State the blood parasite species.
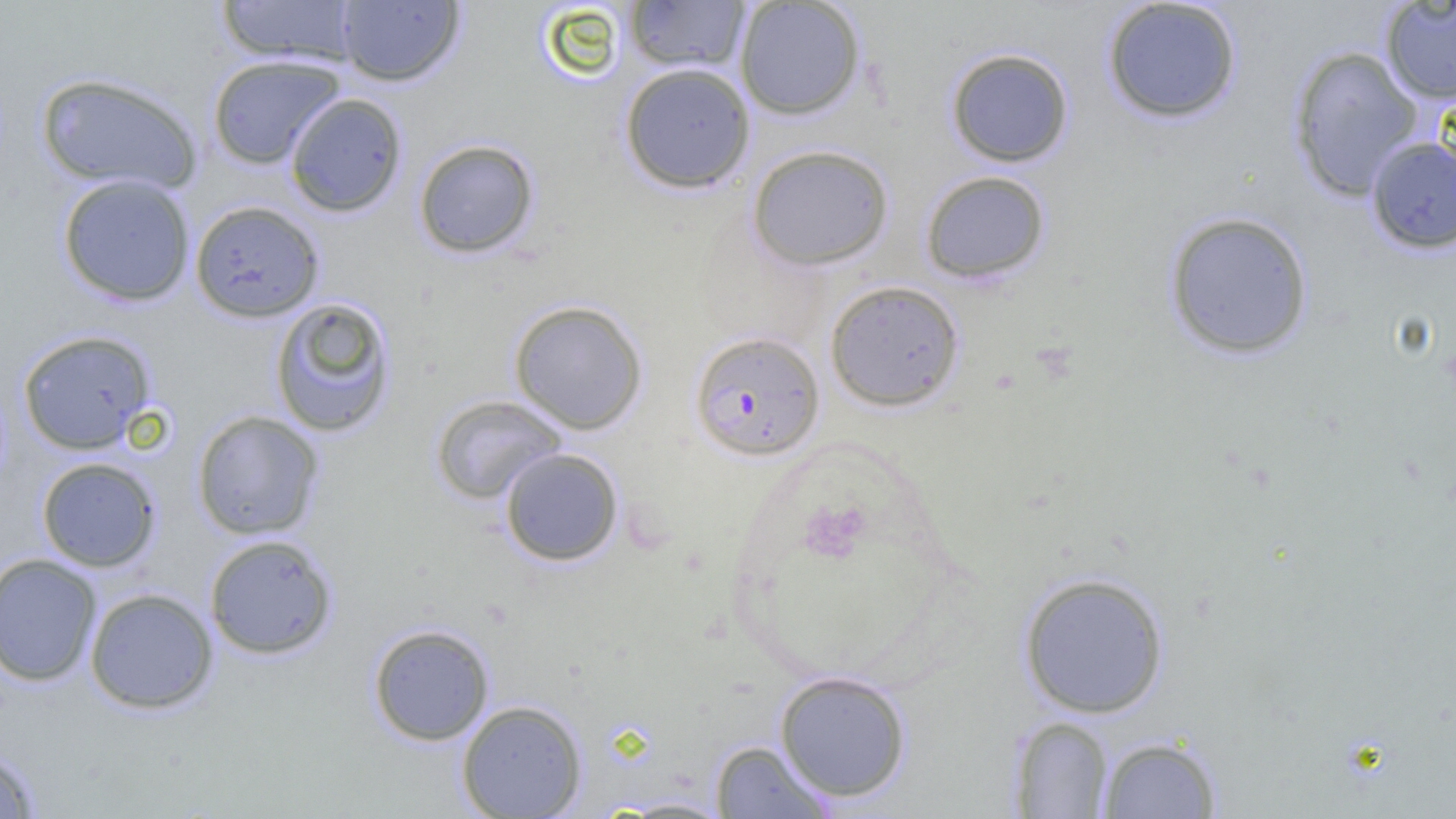

Plasmodium falciparum.

Approximate bounding boxes as [x1, y1, x2, y2] in pixels. Uninfected red blood cell locations: [217, 0, 361, 66], [735, 0, 866, 120], [1102, 0, 1243, 124], [336, 1, 464, 86], [624, 1, 751, 73], [1380, 1, 1456, 105], [1288, 45, 1425, 201], [945, 47, 1075, 168], [206, 54, 345, 170], [619, 62, 756, 194], [35, 71, 203, 194], [284, 92, 407, 218], [1365, 136, 1456, 255], [413, 139, 540, 259], [747, 143, 894, 271], [920, 169, 1051, 285], [57, 174, 196, 306], [190, 199, 325, 322], [1163, 210, 1314, 360], [825, 279, 965, 412], [269, 296, 397, 438], [509, 299, 648, 435], [17, 329, 157, 455], [430, 394, 568, 505], [191, 410, 325, 541], [499, 447, 624, 567], [36, 457, 161, 572], [203, 534, 338, 660], [0, 553, 102, 687], [1017, 571, 1170, 719], [84, 587, 219, 714], [367, 623, 495, 746], [774, 670, 912, 803], [456, 699, 588, 818], [1009, 716, 1115, 818], [1096, 734, 1222, 818], [710, 740, 836, 818], [0, 746, 41, 818], [611, 797, 735, 817]. Plasmodium falciparum-infected red blood cell locations: [689, 330, 824, 462]. Thin blood film. 1000x magnification. Optical microscopy. One field of a larger specimen. Image is 1456×819 pixels.